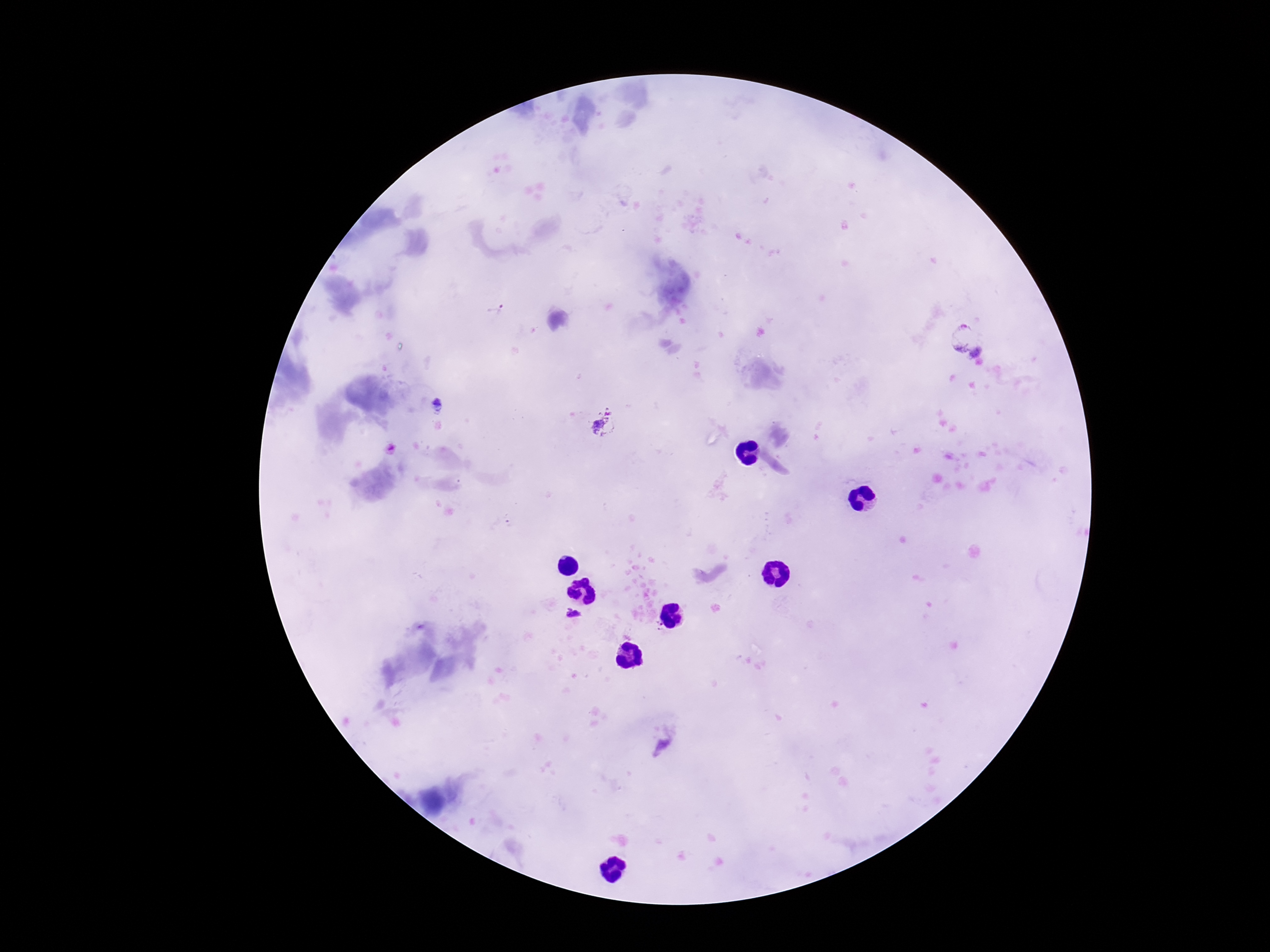

{
  "field_of_view": "one from this slide",
  "preparation": "thick blood smear",
  "plasmodium_parasite_locations": "approximate centers as [x, y] in pixels: [498, 311], [964, 335], [437, 406], [605, 424], [571, 615], [658, 626]",
  "magnification": "100x",
  "patient_malaria_status": "infected",
  "stain": "Giemsa",
  "image_size": "1270×952 pixels",
  "capture": "smartphone camera through the microscope eyepiece"
}